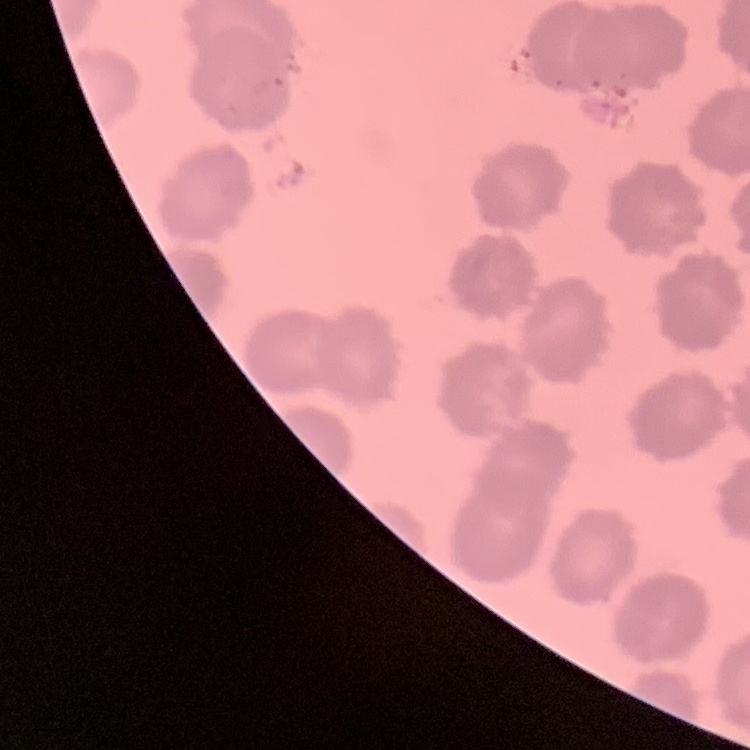

red blood cell morphology = no rouleaux formation
stain = Field's or Giemsa
image type = one tile cut from a larger photomicrograph
preparation = thin peripheral smear